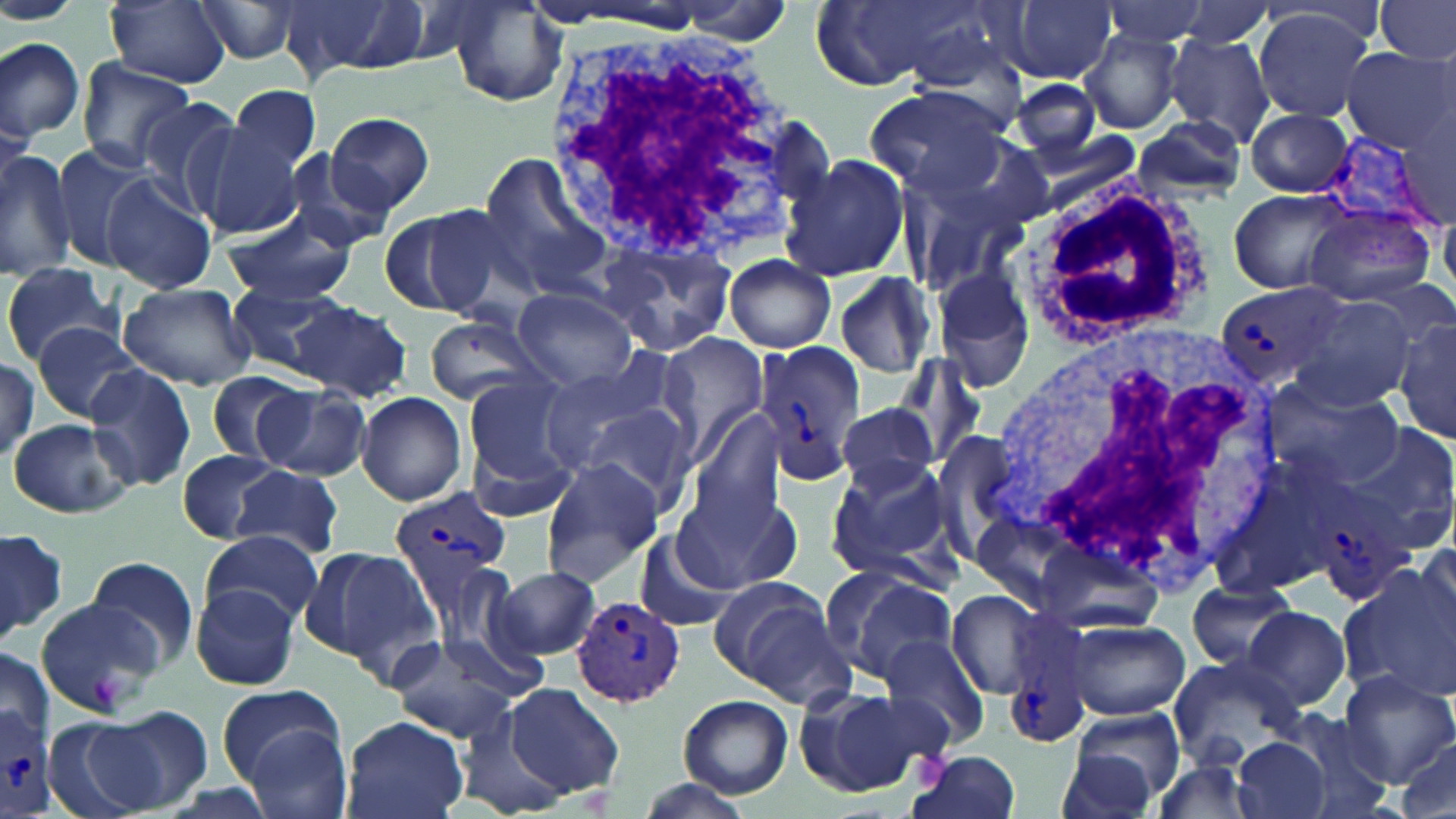
Approximate bounding boxes as (x1, y1, x2, y2) in pixels. Uninfected red blood cell locations: (0, 0, 84, 25), (105, 0, 230, 86), (190, 0, 304, 65), (1008, 0, 1118, 83), (1098, 0, 1216, 48), (1165, 0, 1283, 52), (1377, 0, 1456, 65), (289, 1, 437, 80), (533, 1, 726, 32), (669, 2, 802, 38), (441, 3, 568, 107), (1252, 9, 1379, 123), (1079, 33, 1185, 134), (1161, 34, 1277, 147), (0, 37, 85, 145), (1339, 47, 1453, 153), (77, 58, 196, 169), (1011, 76, 1105, 165), (231, 85, 322, 174), (864, 86, 1013, 201), (133, 96, 245, 212), (1243, 108, 1353, 197), (325, 111, 434, 214), (0, 117, 30, 212), (1129, 119, 1249, 203), (186, 124, 305, 239), (0, 144, 78, 280), (49, 144, 153, 263), (280, 152, 396, 253), (477, 155, 611, 294), (780, 156, 912, 283), (898, 170, 1031, 304), (100, 174, 217, 294), (1228, 188, 1353, 296), (1300, 203, 1437, 307), (388, 205, 517, 319), (221, 211, 358, 305), (594, 237, 738, 357), (723, 256, 837, 351), (2, 261, 124, 365), (929, 269, 1037, 397), (832, 272, 942, 379), (118, 283, 257, 390), (224, 284, 347, 377), (510, 287, 640, 391), (1291, 293, 1422, 411), (288, 300, 411, 400), (422, 316, 548, 405), (1394, 320, 1456, 446), (31, 323, 145, 423), (653, 333, 772, 468), (892, 354, 987, 470), (83, 362, 196, 491), (535, 363, 674, 470), (206, 372, 308, 463), (461, 376, 581, 492), (1262, 376, 1403, 488), (256, 384, 372, 480), (356, 391, 467, 505), (573, 401, 704, 523), (831, 404, 941, 491), (685, 408, 788, 531), (8, 417, 134, 519), (1340, 424, 1455, 553), (464, 428, 579, 525), (174, 450, 277, 542), (1216, 451, 1359, 593), (825, 457, 956, 579), (538, 458, 664, 587), (232, 465, 344, 559), (673, 489, 787, 597), (0, 525, 68, 647), (201, 528, 323, 627), (635, 532, 736, 630), (1417, 538, 1456, 641), (1032, 539, 1167, 638), (310, 547, 443, 668), (84, 555, 201, 668), (495, 566, 599, 659), (1337, 567, 1455, 700), (823, 568, 962, 681), (1187, 579, 1300, 673), (708, 580, 851, 703), (190, 584, 301, 691), (946, 587, 1051, 700), (33, 588, 171, 716), (1241, 608, 1351, 710), (1065, 620, 1188, 719), (880, 633, 991, 750), (387, 640, 524, 742), (0, 647, 54, 750), (1165, 657, 1306, 766), (1336, 668, 1456, 788), (503, 682, 624, 799), (217, 684, 345, 783), (797, 687, 939, 795), (677, 694, 793, 798), (454, 705, 569, 817), (1066, 706, 1189, 808), (95, 707, 213, 815), (37, 710, 162, 818), (1278, 712, 1396, 819), (339, 715, 468, 819), (244, 725, 354, 819), (1228, 734, 1334, 819), (1392, 737, 1454, 819), (1053, 746, 1159, 819), (907, 752, 1023, 819), (1148, 757, 1263, 819), (635, 776, 755, 819). Platelet locations: (86, 671, 127, 703), (915, 752, 950, 788). White blood cell locations: (536, 25, 814, 266), (1031, 184, 1210, 344), (989, 319, 1281, 598). Plasmodium vivax-infected red blood cell locations: (1334, 120, 1454, 239), (1214, 282, 1349, 390), (755, 345, 865, 485), (1306, 471, 1417, 603), (389, 486, 513, 598), (574, 594, 685, 707), (1002, 629, 1098, 750), (0, 704, 56, 810). Slide-level diagnosis: Plasmodium vivax. Image is 1456×819 pixels. One field of a larger specimen. May-Grünwald-Giemsa-stained preparation. Thin blood film. Captured at 1000x magnification. Light microscopy.